Identify the cell.
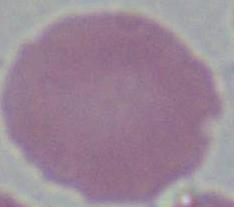
An erythrocyte.

magnification = 1000x
modality = photomicrograph